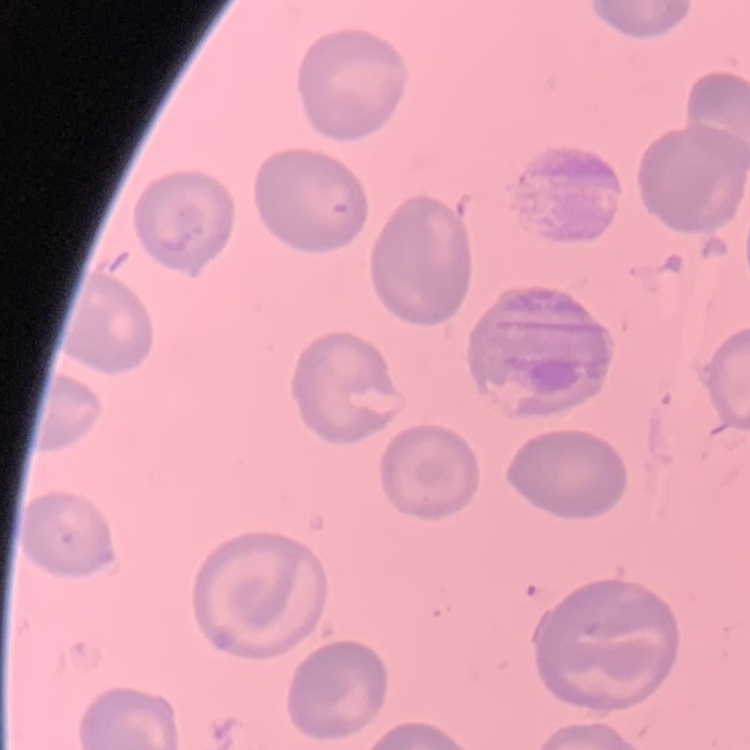
{
  "erythrocyte_morphology": "no rouleaux formation",
  "preparation": "thin blood smear",
  "image_type": "one tile cut from a larger photomicrograph",
  "stain": "Field's or Giemsa"
}